Point out each leukocyte.
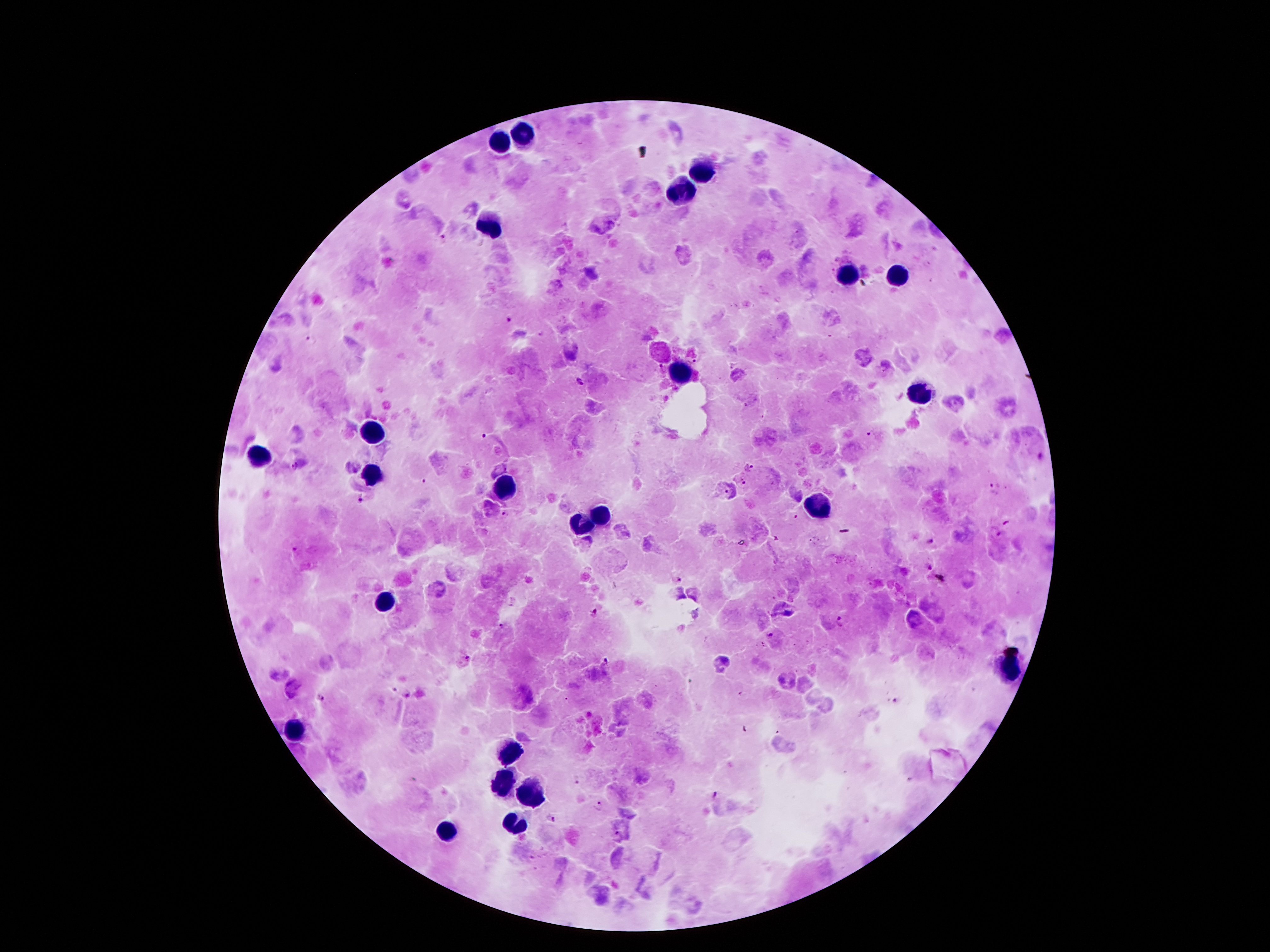

Approximate centers as (x, y) in pixels.
Leukocytes: (528, 137), (498, 143), (706, 173), (681, 194), (486, 228), (851, 272), (901, 276), (679, 373), (918, 396), (376, 434), (255, 455), (376, 475), (507, 488), (815, 507), (603, 518), (578, 528), (385, 600), (1007, 675), (291, 732), (507, 751), (503, 780), (532, 793), (517, 820), (446, 831).

Plasmodium parasite locations = (445, 240), (509, 320), (312, 339), (579, 381), (871, 433), (485, 436), (294, 466), (749, 467), (740, 481), (424, 482), (994, 483), (358, 500), (505, 514), (995, 531), (931, 541), (929, 567), (680, 579), (597, 612), (841, 621), (503, 627), (769, 634), (467, 659), (605, 659), (410, 693), (319, 697), (895, 698), (743, 729), (577, 780), (717, 797), (600, 805), (551, 818)
stain = Giemsa
image size = 1270×952 pixels
patient malaria status = positive for Plasmodium falciparum
preparation = thick peripheral-blood smear
capture = smartphone through the microscope eyepiece
magnification = 100x
field of view = one from this slide